Outline each blood parasite and name the species.
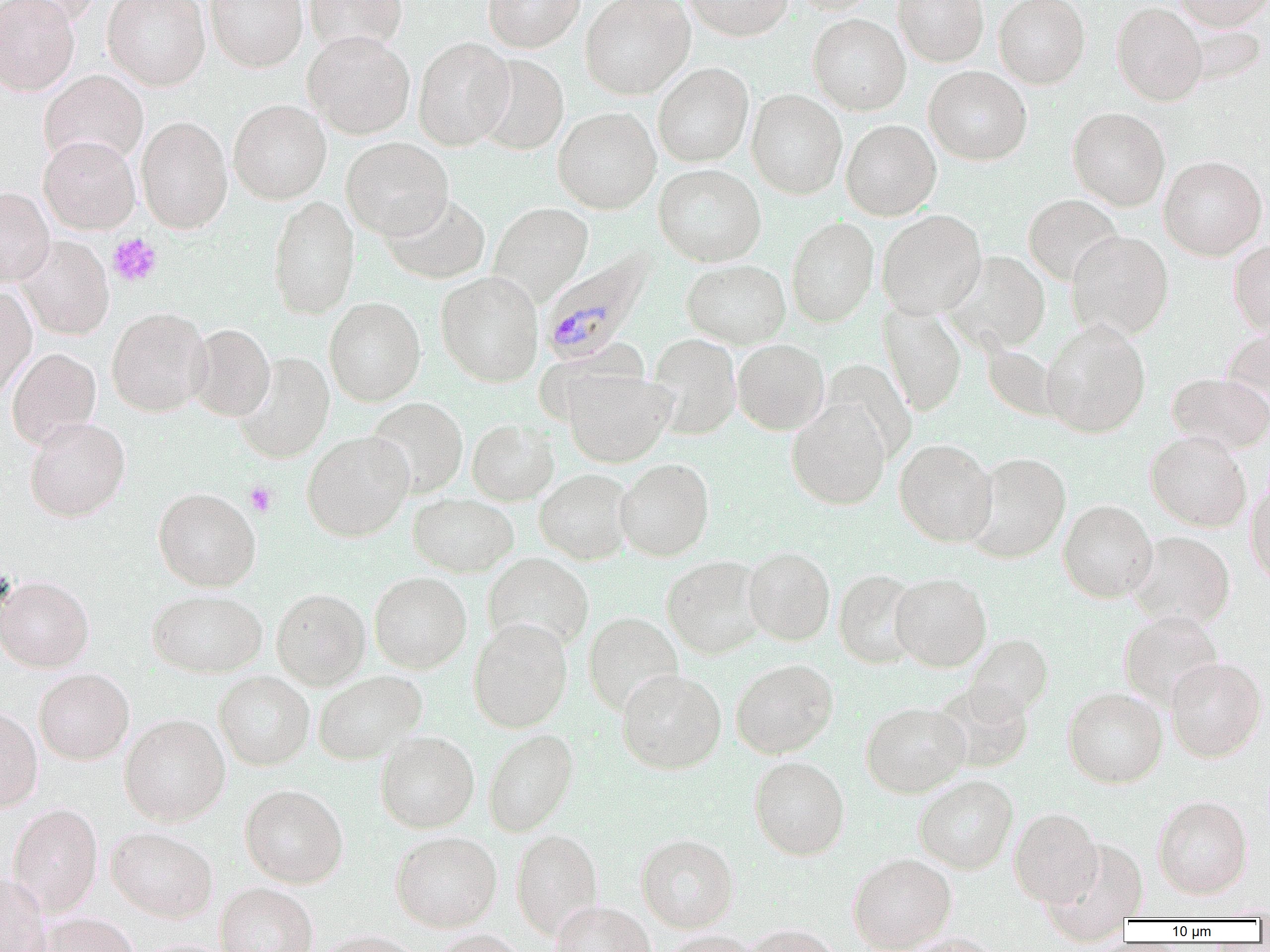

Approximate bounding boxes as named x1/y1/x2/y2 corners in pixels.
Plasmodium malariae-infected red blood cells: (x1=540, y1=249, x2=656, y2=365).
No Plasmodium falciparum, Plasmodium ovale, Plasmodium vivax, Babesia divergens, or Trypanosoma brucei observed.

Uninfected red blood cell locations: (x1=0, y1=0, x2=79, y2=95), (x1=3, y1=0, x2=103, y2=26), (x1=102, y1=0, x2=210, y2=90), (x1=205, y1=0, x2=308, y2=71), (x1=304, y1=0, x2=407, y2=56), (x1=483, y1=0, x2=585, y2=52), (x1=580, y1=0, x2=694, y2=99), (x1=684, y1=0, x2=793, y2=41), (x1=787, y1=0, x2=880, y2=15), (x1=893, y1=0, x2=988, y2=66), (x1=994, y1=0, x2=1090, y2=89), (x1=1174, y1=0, x2=1270, y2=32), (x1=1111, y1=2, x2=1208, y2=106), (x1=807, y1=14, x2=910, y2=115), (x1=303, y1=31, x2=415, y2=139), (x1=413, y1=37, x2=515, y2=150), (x1=474, y1=54, x2=569, y2=155), (x1=653, y1=62, x2=754, y2=167), (x1=924, y1=66, x2=1032, y2=165), (x1=39, y1=70, x2=149, y2=168), (x1=747, y1=89, x2=847, y2=199), (x1=228, y1=99, x2=331, y2=204), (x1=553, y1=107, x2=661, y2=214), (x1=1067, y1=107, x2=1170, y2=210), (x1=135, y1=116, x2=232, y2=234), (x1=841, y1=119, x2=941, y2=220), (x1=39, y1=134, x2=140, y2=234), (x1=341, y1=137, x2=453, y2=239), (x1=1159, y1=155, x2=1267, y2=260), (x1=653, y1=164, x2=766, y2=266), (x1=0, y1=187, x2=54, y2=286), (x1=381, y1=194, x2=490, y2=283), (x1=1023, y1=194, x2=1122, y2=285), (x1=267, y1=195, x2=359, y2=318), (x1=489, y1=201, x2=593, y2=304), (x1=876, y1=210, x2=987, y2=319), (x1=786, y1=216, x2=879, y2=327), (x1=1066, y1=231, x2=1174, y2=340), (x1=17, y1=236, x2=114, y2=340), (x1=1229, y1=239, x2=1270, y2=336), (x1=944, y1=251, x2=1050, y2=354), (x1=681, y1=259, x2=791, y2=348), (x1=435, y1=271, x2=543, y2=387), (x1=0, y1=286, x2=37, y2=401), (x1=324, y1=297, x2=426, y2=406), (x1=879, y1=303, x2=967, y2=416), (x1=106, y1=307, x2=210, y2=416), (x1=1041, y1=320, x2=1151, y2=438), (x1=1221, y1=323, x2=1270, y2=417), (x1=187, y1=324, x2=274, y2=420), (x1=647, y1=333, x2=742, y2=440), (x1=732, y1=339, x2=829, y2=435), (x1=982, y1=345, x2=1061, y2=421), (x1=7, y1=347, x2=101, y2=448), (x1=234, y1=352, x2=335, y2=463), (x1=561, y1=368, x2=677, y2=467), (x1=1167, y1=372, x2=1270, y2=455), (x1=366, y1=397, x2=468, y2=497), (x1=786, y1=399, x2=891, y2=510), (x1=24, y1=417, x2=130, y2=522), (x1=467, y1=418, x2=559, y2=505), (x1=302, y1=430, x2=414, y2=542), (x1=1146, y1=431, x2=1252, y2=532), (x1=894, y1=439, x2=997, y2=546), (x1=967, y1=452, x2=1071, y2=563), (x1=615, y1=458, x2=714, y2=561), (x1=534, y1=469, x2=634, y2=564), (x1=1245, y1=478, x2=1270, y2=588), (x1=153, y1=487, x2=261, y2=592), (x1=408, y1=493, x2=518, y2=577), (x1=1058, y1=499, x2=1158, y2=602), (x1=1129, y1=531, x2=1235, y2=629), (x1=743, y1=547, x2=835, y2=646), (x1=483, y1=552, x2=594, y2=652), (x1=662, y1=555, x2=765, y2=659), (x1=833, y1=569, x2=922, y2=668), (x1=369, y1=571, x2=472, y2=673), (x1=890, y1=572, x2=992, y2=671), (x1=0, y1=575, x2=94, y2=672), (x1=271, y1=587, x2=370, y2=690), (x1=147, y1=588, x2=267, y2=678), (x1=1119, y1=610, x2=1223, y2=709), (x1=583, y1=612, x2=683, y2=715), (x1=468, y1=618, x2=572, y2=733), (x1=965, y1=634, x2=1052, y2=719), (x1=1165, y1=656, x2=1267, y2=762), (x1=730, y1=659, x2=838, y2=758), (x1=34, y1=668, x2=134, y2=764), (x1=616, y1=668, x2=727, y2=774), (x1=313, y1=670, x2=427, y2=765), (x1=214, y1=671, x2=314, y2=769), (x1=932, y1=681, x2=1035, y2=773), (x1=1063, y1=687, x2=1167, y2=788), (x1=861, y1=701, x2=969, y2=797), (x1=0, y1=703, x2=43, y2=812), (x1=119, y1=713, x2=230, y2=826), (x1=482, y1=728, x2=579, y2=837), (x1=375, y1=729, x2=479, y2=833), (x1=749, y1=755, x2=850, y2=860), (x1=914, y1=774, x2=1018, y2=873), (x1=240, y1=784, x2=348, y2=888), (x1=1153, y1=794, x2=1253, y2=899), (x1=7, y1=803, x2=103, y2=916), (x1=1009, y1=806, x2=1103, y2=906), (x1=106, y1=826, x2=218, y2=922), (x1=510, y1=829, x2=603, y2=938), (x1=390, y1=830, x2=502, y2=932), (x1=636, y1=834, x2=739, y2=932), (x1=847, y1=852, x2=957, y2=952), (x1=0, y1=872, x2=51, y2=952), (x1=215, y1=882, x2=318, y2=952), (x1=549, y1=901, x2=656, y2=952), (x1=37, y1=912, x2=140, y2=952), (x1=740, y1=924, x2=841, y2=951), (x1=314, y1=929, x2=426, y2=952), (x1=431, y1=930, x2=527, y2=952), (x1=659, y1=931, x2=763, y2=952). Platelet locations: (x1=108, y1=233, x2=162, y2=287), (x1=245, y1=481, x2=277, y2=516). Slide-level diagnosis: Plasmodium malariae. Thin blood film. Single field of view. 1000x magnification. Image is 1270×952 pixels. Optical microscopy.